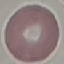

result: negative for malaria parasites
capture: smartphone camera at the microscope eyepiece
image_type: automatically extracted cell patch, resized to 64 × 64 pixels
stain: Giemsa
preparation: thin blood film